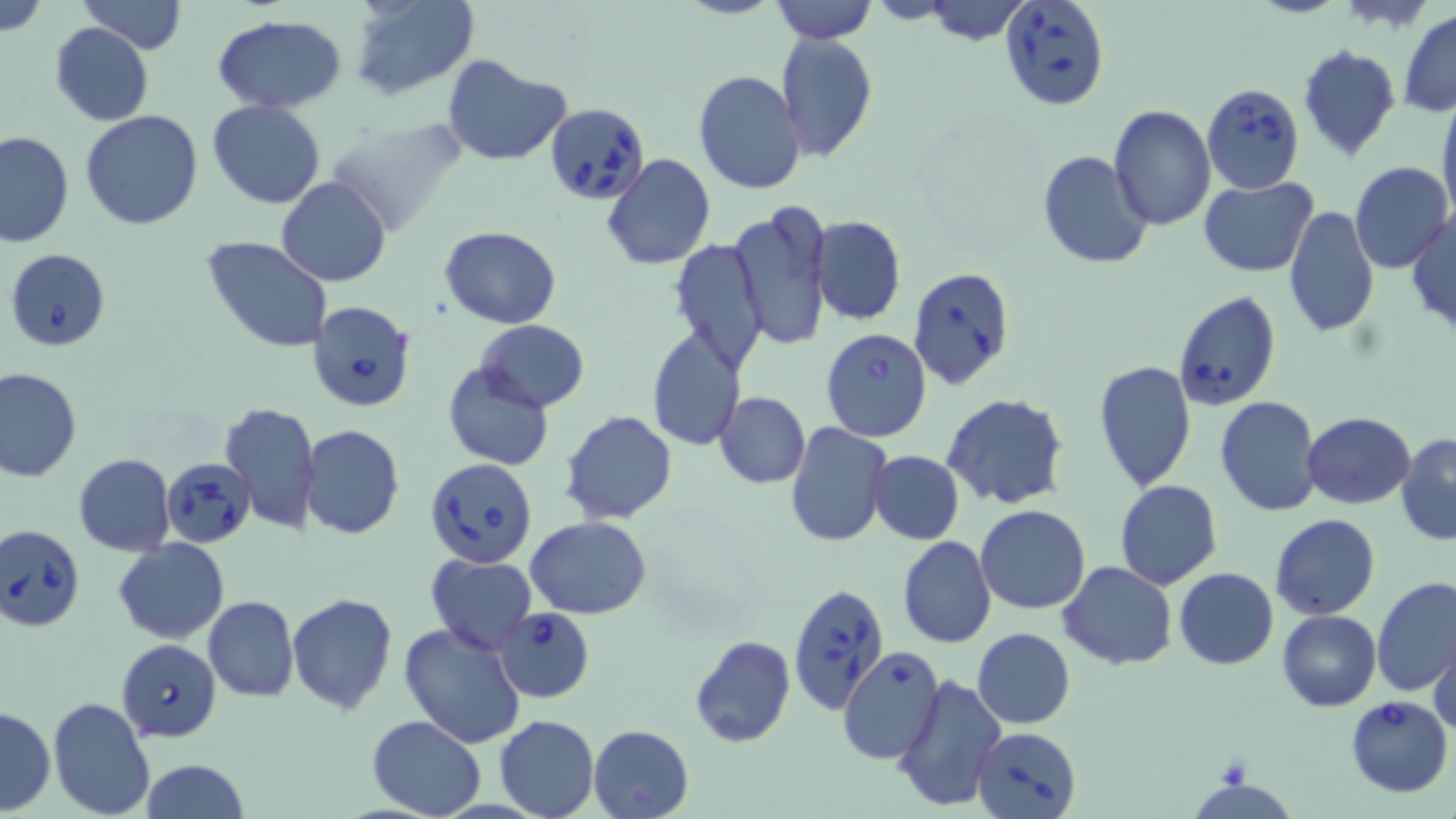

Summary:
  - Coordinate format: approximate bounding boxes as named x1/y1/x2/y2 corners in pixels
  - Babesia divergens-infected red blood cell locations: (x1=998, y1=0, x2=1110, y2=111), (x1=1203, y1=84, x2=1304, y2=193), (x1=546, y1=102, x2=651, y2=204), (x1=5, y1=250, x2=111, y2=349), (x1=910, y1=266, x2=1015, y2=390), (x1=1173, y1=290, x2=1281, y2=411), (x1=304, y1=299, x2=416, y2=414), (x1=160, y1=456, x2=256, y2=548), (x1=425, y1=456, x2=538, y2=568), (x1=1, y1=523, x2=85, y2=633), (x1=787, y1=583, x2=890, y2=714), (x1=492, y1=605, x2=595, y2=701), (x1=119, y1=641, x2=224, y2=741), (x1=1345, y1=696, x2=1452, y2=797), (x1=973, y1=727, x2=1081, y2=819)
  - Uninfected red blood cell locations: (x1=78, y1=0, x2=186, y2=54), (x1=351, y1=0, x2=476, y2=99), (x1=769, y1=0, x2=877, y2=43), (x1=0, y1=1, x2=48, y2=38), (x1=915, y1=1, x2=1037, y2=44), (x1=1399, y1=10, x2=1456, y2=117), (x1=212, y1=14, x2=346, y2=111), (x1=49, y1=23, x2=154, y2=126), (x1=775, y1=32, x2=878, y2=162), (x1=1297, y1=45, x2=1401, y2=161), (x1=442, y1=55, x2=570, y2=165), (x1=693, y1=70, x2=806, y2=195), (x1=1437, y1=91, x2=1456, y2=225), (x1=206, y1=100, x2=326, y2=209), (x1=1107, y1=103, x2=1215, y2=230), (x1=80, y1=110, x2=204, y2=229), (x1=0, y1=129, x2=74, y2=249), (x1=1038, y1=150, x2=1153, y2=271), (x1=602, y1=153, x2=716, y2=270), (x1=1349, y1=161, x2=1454, y2=275), (x1=277, y1=177, x2=391, y2=289), (x1=1198, y1=177, x2=1318, y2=277), (x1=729, y1=202, x2=831, y2=351), (x1=1283, y1=206, x2=1380, y2=339), (x1=1408, y1=210, x2=1456, y2=336), (x1=810, y1=216, x2=906, y2=324), (x1=440, y1=226, x2=561, y2=328), (x1=201, y1=236, x2=333, y2=353), (x1=669, y1=239, x2=769, y2=373), (x1=474, y1=320, x2=590, y2=413), (x1=822, y1=327, x2=932, y2=443), (x1=645, y1=328, x2=744, y2=448), (x1=1093, y1=360, x2=1197, y2=492), (x1=442, y1=362, x2=553, y2=472), (x1=0, y1=366, x2=82, y2=482), (x1=715, y1=391, x2=810, y2=488), (x1=943, y1=394, x2=1069, y2=510), (x1=1214, y1=395, x2=1322, y2=516), (x1=219, y1=399, x2=321, y2=534), (x1=560, y1=411, x2=676, y2=525), (x1=1303, y1=413, x2=1415, y2=509), (x1=785, y1=423, x2=891, y2=547), (x1=300, y1=424, x2=404, y2=540), (x1=1396, y1=434, x2=1456, y2=547), (x1=868, y1=450, x2=965, y2=545), (x1=72, y1=453, x2=175, y2=557), (x1=1114, y1=479, x2=1223, y2=589), (x1=976, y1=504, x2=1090, y2=614), (x1=1270, y1=513, x2=1379, y2=619), (x1=526, y1=517, x2=653, y2=618), (x1=895, y1=535, x2=997, y2=649), (x1=114, y1=538, x2=229, y2=643), (x1=426, y1=555, x2=537, y2=654), (x1=1059, y1=561, x2=1177, y2=671), (x1=1173, y1=566, x2=1278, y2=669), (x1=1372, y1=577, x2=1456, y2=699), (x1=287, y1=593, x2=397, y2=716), (x1=1281, y1=594, x2=1456, y2=703), (x1=203, y1=596, x2=298, y2=703), (x1=1277, y1=610, x2=1381, y2=712), (x1=397, y1=621, x2=529, y2=750), (x1=972, y1=628, x2=1075, y2=728), (x1=1430, y1=633, x2=1456, y2=739), (x1=688, y1=635, x2=795, y2=749), (x1=838, y1=647, x2=947, y2=765), (x1=892, y1=673, x2=1007, y2=814), (x1=47, y1=696, x2=156, y2=819), (x1=1, y1=705, x2=55, y2=815), (x1=367, y1=715, x2=487, y2=819), (x1=494, y1=715, x2=598, y2=819), (x1=589, y1=725, x2=693, y2=818), (x1=140, y1=759, x2=251, y2=819)
  - Slide-level diagnosis: Babesia divergens
  - Magnification: 1000x
  - Modality: optical microscopy
  - Field of view: one of a larger specimen
  - Preparation: thin blood film
  - Image size: 1456×819 pixels
  - Stain: May-Grünwald-Giemsa